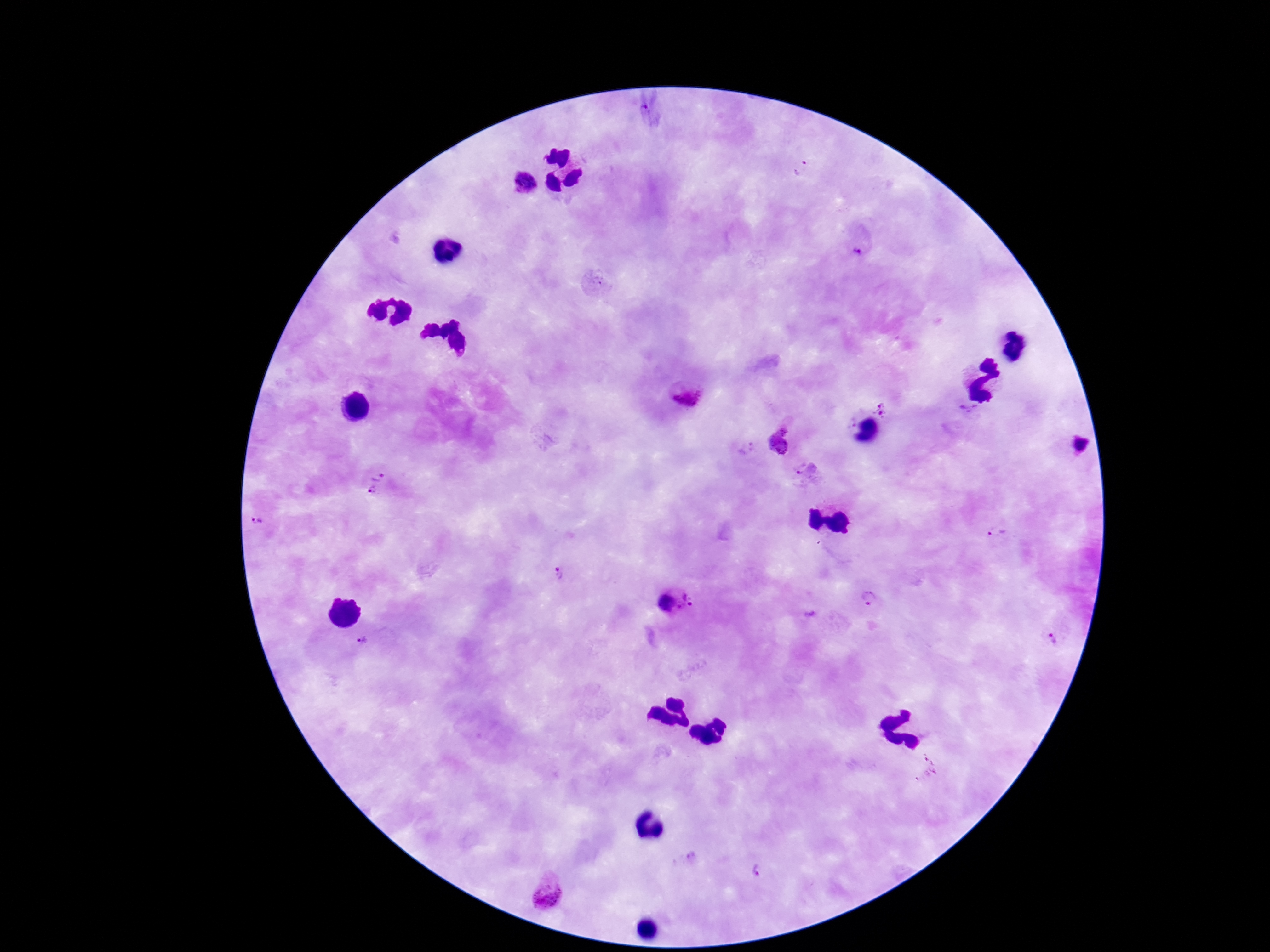

{
  "capture": "smartphone camera through the microscope eyepiece",
  "magnification": "100x",
  "image_size": "1270×952 pixels",
  "field_of_view": "single",
  "patient_malaria_status": "infected",
  "plasmodium_parasite_locations": "approximate object centers, in pixels from the top-left corner: (x=799, y=167), (x=525, y=183), (x=858, y=250), (x=695, y=396), (x=882, y=409), (x=968, y=409), (x=777, y=444), (x=804, y=470), (x=378, y=473), (x=372, y=490), (x=255, y=521), (x=998, y=531), (x=557, y=573), (x=870, y=600), (x=674, y=602), (x=1056, y=638), (x=361, y=643), (x=691, y=855), (x=755, y=870), (x=547, y=892)",
  "preparation": "thick peripheral-blood smear",
  "stain": "Giemsa"
}